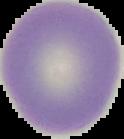
The area outside the segmented cell region is set to black. From a thin blood film. Malaria status: uninfected. Image is 124×139 pixels.